Classify this cell by malaria status.
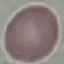
It is uninfected.

Summary:
  - Preparation: thin smear
  - Stain: Giemsa
  - Image type: cell patch, automatically extracted from a larger field of view and resized to 64 × 64 pixels
  - Capture: smartphone camera at the microscope eyepiece